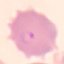
Summary:
  - Malaria status: parasitized
  - Capture: smartphone camera at the microscope eyepiece
  - Image type: automatically extracted cell patch, resized to 64 × 64 pixels
  - Stain: Giemsa
  - Preparation: thin blood smear